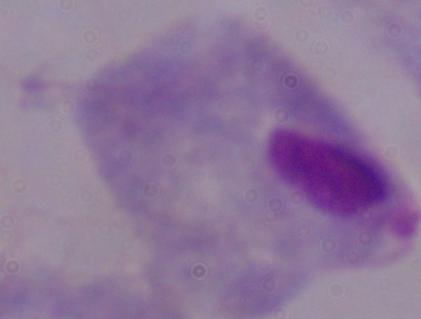

Summary:
  - Identification: trichomonad
  - Magnification: 1000x
  - Modality: photomicrograph